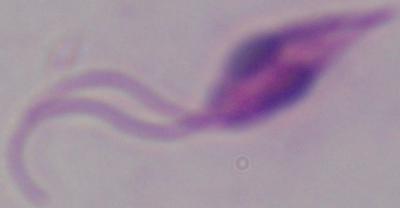

Micrograph. 1000x magnification. A Leishmania parasite is shown.